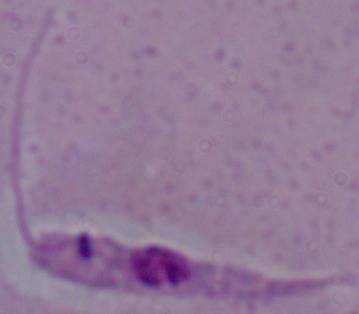
Summary:
  - Magnification: 1000x
  - Identification: Leishmania
  - Modality: micrograph